Locate every blood parasite and identify its species.
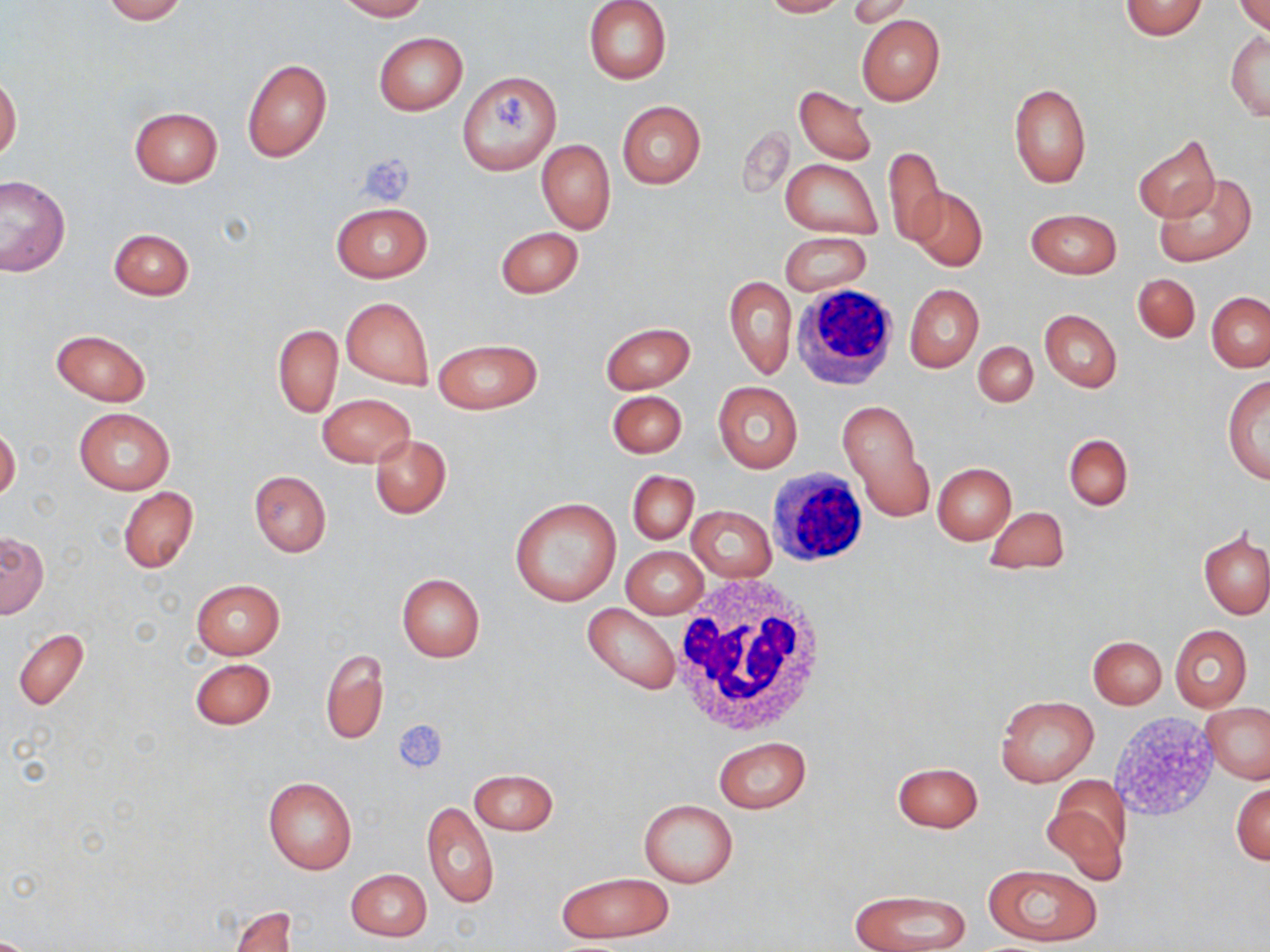
No blood parasites seen.

Approximate bounding boxes as (x1, y1, x2, y2) in pixels. Uninfected red blood cell locations: (100, 0, 190, 23), (337, 0, 427, 21), (583, 0, 672, 84), (762, 0, 845, 17), (848, 1, 912, 29), (1118, 1, 1208, 39), (1234, 2, 1270, 35), (856, 15, 945, 105), (372, 31, 468, 115), (1226, 32, 1269, 120), (241, 58, 332, 163), (457, 71, 561, 175), (0, 73, 21, 163), (1008, 83, 1091, 188), (793, 86, 878, 165), (617, 101, 706, 190), (129, 106, 222, 187), (739, 126, 794, 199), (1132, 136, 1220, 222), (537, 139, 614, 234), (882, 145, 946, 248), (780, 158, 882, 239), (1154, 174, 1257, 265), (0, 175, 69, 277), (909, 186, 987, 270), (331, 203, 432, 282), (1026, 207, 1122, 279), (495, 225, 583, 299), (108, 227, 193, 301), (781, 232, 871, 296), (1132, 272, 1200, 343), (724, 274, 797, 380), (904, 284, 984, 373), (1207, 291, 1270, 372), (341, 297, 434, 390), (1039, 309, 1122, 392), (600, 322, 694, 393), (273, 324, 343, 418), (50, 329, 152, 407), (432, 338, 542, 414), (973, 341, 1037, 408), (1222, 376, 1270, 484), (714, 382, 803, 473), (607, 390, 687, 458), (317, 393, 415, 467), (838, 398, 934, 524), (74, 406, 174, 495), (0, 424, 20, 503), (369, 433, 452, 518), (1064, 434, 1133, 510), (931, 463, 1015, 544), (249, 470, 331, 556), (627, 471, 698, 543), (119, 486, 198, 574), (509, 495, 622, 607), (983, 505, 1071, 575), (688, 506, 775, 582), (1, 531, 48, 618), (1200, 532, 1270, 618), (622, 547, 707, 619), (397, 573, 485, 661), (191, 579, 285, 658), (583, 602, 680, 694), (1170, 625, 1251, 712), (12, 628, 89, 709), (1088, 635, 1167, 708), (321, 649, 387, 746), (191, 658, 275, 729), (995, 695, 1098, 787), (1201, 702, 1270, 783), (715, 736, 809, 814), (891, 761, 983, 832), (468, 769, 557, 835), (263, 776, 358, 876), (1042, 779, 1130, 882), (1231, 783, 1270, 865), (637, 799, 739, 888), (422, 800, 498, 909), (983, 865, 1103, 947), (345, 868, 432, 941), (557, 871, 674, 943), (849, 889, 972, 952), (228, 905, 298, 952). Platelet locations: (491, 89, 531, 133), (359, 154, 414, 206), (393, 720, 447, 773). White blood cell locations: (791, 283, 902, 393), (769, 467, 870, 565), (667, 576, 833, 738). Slide-level diagnosis: no evidence of blood parasites. Image is 1270×952 pixels. May-Grünwald-Giemsa-stained preparation. Thin blood film. Light microscopy. 1000x magnification. One field of a larger specimen.